Assess this cell for malaria.
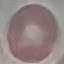

It is uninfected.

Summary:
  - Image type: automatically extracted cell patch, resized to 64 × 64 pixels
  - Capture: smartphone through the microscope eyepiece
  - Stain: Giemsa
  - Preparation: thin blood smear